Give the preparation type.
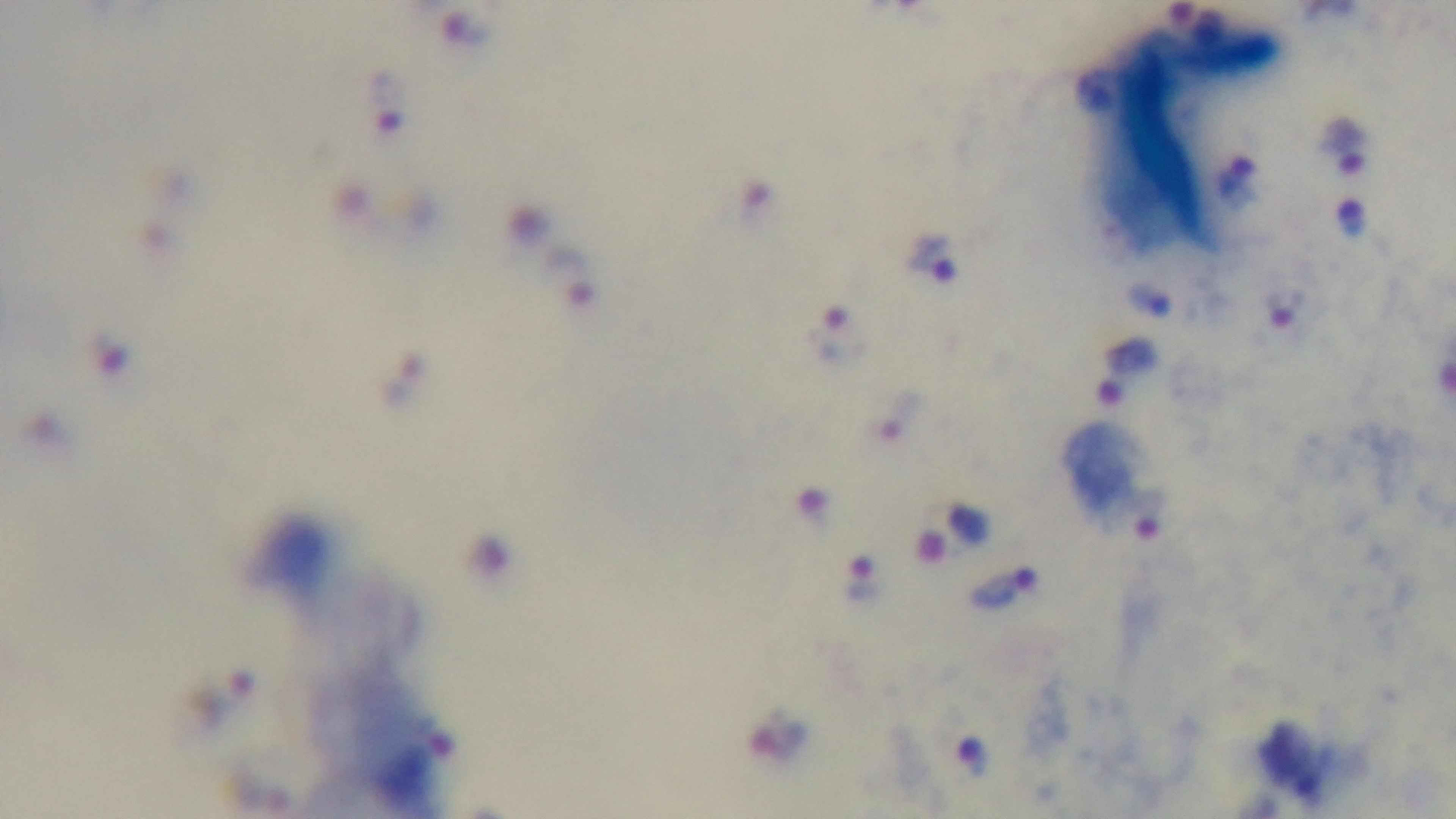

It is a thick blood film.

malaria status = positive
objective = 100x oil immersion
capture = mounted 4K digital camera
modality = light microscopy
stain = Giemsa
field of view = one from the slide